State the blood parasite species.
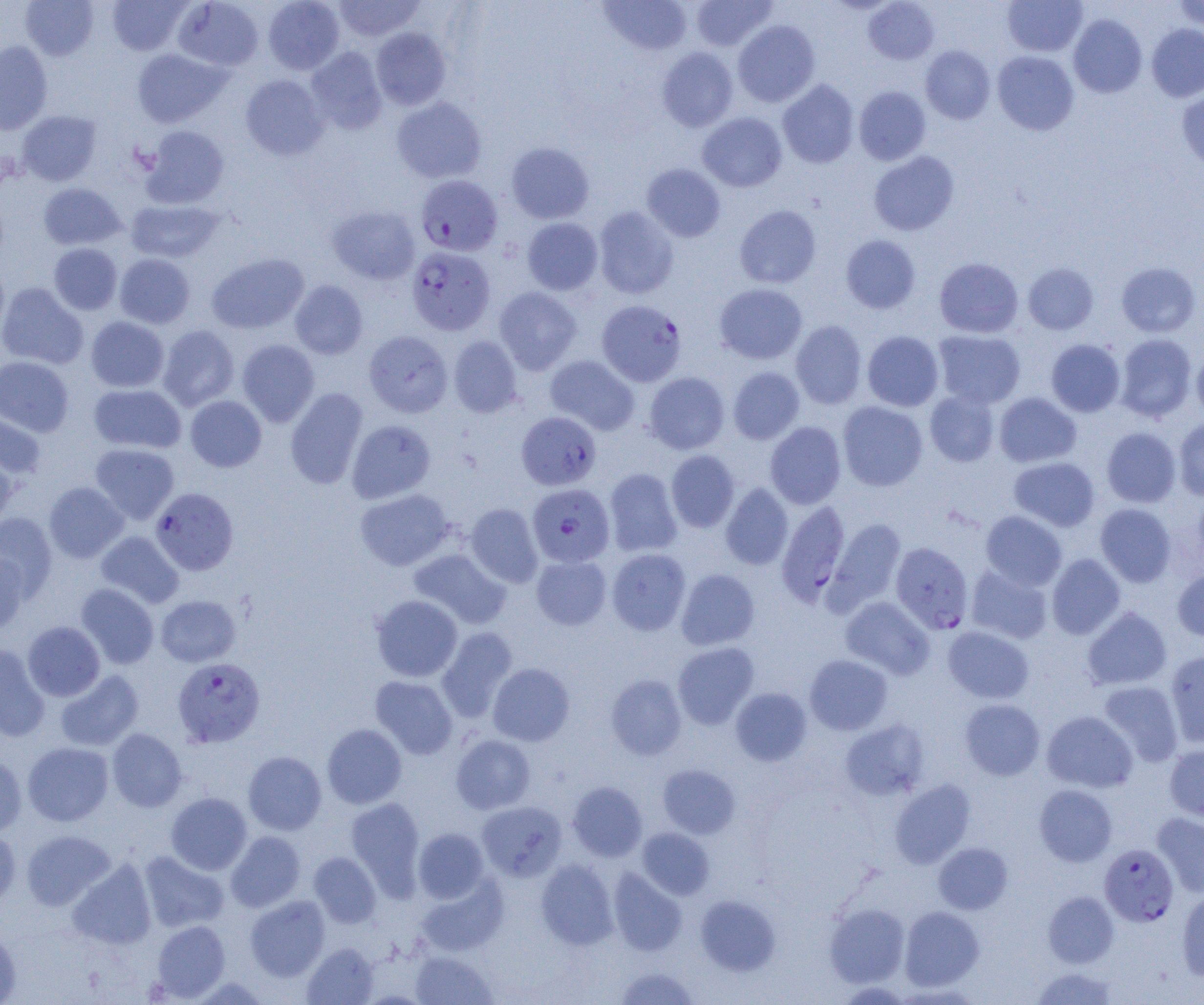

Plasmodium falciparum.

Summary:
  - Coordinate format: approximate bounding boxes as (x1,y1)-(x2,y2) corner pairs in pixels
  - Uninfected red blood cell locations: (20,0)-(99,60), (107,0)-(192,56), (263,0)-(344,74), (333,0)-(425,42), (689,0)-(777,51), (863,0)-(939,65), (1003,0)-(1088,57), (173,1)-(264,71), (599,1)-(693,56), (1173,1)-(1204,30), (1068,14)-(1147,98), (733,20)-(820,107), (1146,24)-(1204,103), (371,27)-(451,110), (0,41)-(53,135), (920,45)-(996,124), (306,46)-(387,134), (656,47)-(738,132), (132,49)-(229,127), (992,51)-(1079,135), (240,74)-(328,160), (777,79)-(859,168), (854,86)-(931,165), (1176,87)-(1204,170), (391,97)-(487,183), (17,111)-(101,186), (697,112)-(787,192), (141,125)-(230,209), (506,142)-(594,223), (869,151)-(960,236), (641,163)-(726,242), (38,183)-(127,250), (126,199)-(224,263), (593,205)-(679,299), (734,205)-(821,289), (326,206)-(420,285), (522,217)-(603,295), (840,234)-(921,314), (49,243)-(122,315), (207,253)-(309,334), (114,254)-(195,328), (934,257)-(1023,338), (1116,262)-(1201,337), (0,263)-(9,337), (1023,263)-(1098,335), (289,280)-(368,359), (0,283)-(88,370), (714,283)-(807,364), (494,286)-(582,375), (86,316)-(169,392), (791,320)-(867,409), (158,325)-(239,411), (363,330)-(453,418), (862,330)-(944,411), (933,330)-(1026,409), (1115,334)-(1197,422), (448,336)-(522,418), (237,339)-(320,426), (1045,339)-(1125,417), (1192,350)-(1204,421), (545,355)-(640,435), (0,356)-(74,437), (728,367)-(804,445), (644,372)-(730,454), (89,384)-(186,454), (285,387)-(368,490), (925,391)-(1000,467), (994,392)-(1081,468), (185,396)-(267,472), (838,401)-(928,491), (0,411)-(46,480), (1174,417)-(1204,500), (347,420)-(435,503), (765,421)-(846,509), (1101,427)-(1181,507), (90,443)-(179,524), (666,450)-(740,532), (0,455)-(16,533), (1009,457)-(1100,532), (604,468)-(682,557), (44,482)-(128,563), (720,483)-(793,570), (354,488)-(455,571), (1192,489)-(1204,568), (465,503)-(543,588), (1095,503)-(1176,587), (981,510)-(1067,590), (0,512)-(58,598), (825,518)-(907,614), (96,531)-(184,608), (606,548)-(691,636), (409,549)-(511,629), (0,551)-(30,635), (531,554)-(611,629), (1046,554)-(1125,639), (966,565)-(1053,644), (1172,568)-(1204,641), (676,569)-(759,650), (76,583)-(159,669), (156,595)-(241,667), (371,595)-(462,681), (840,597)-(934,679), (1082,606)-(1172,690), (22,621)-(105,701), (943,626)-(1034,703), (438,627)-(518,722), (672,642)-(759,729), (0,643)-(49,742), (1164,650)-(1204,747), (804,654)-(892,735), (487,663)-(575,746), (55,669)-(143,751), (605,674)-(687,760), (370,675)-(458,759), (1098,680)-(1184,767), (730,687)-(812,766), (960,698)-(1045,780), (1041,710)-(1138,793), (839,719)-(930,800), (322,724)-(407,809), (107,728)-(187,812), (451,734)-(536,814), (23,742)-(114,826), (1164,744)-(1204,822), (243,751)-(326,835), (0,755)-(27,838), (658,764)-(740,839), (888,779)-(975,868), (567,781)-(647,862), (1034,784)-(1117,867), (166,792)-(252,875), (346,797)-(425,894), (477,801)-(567,881), (1152,812)-(1204,897), (637,827)-(715,900), (413,828)-(489,903), (0,830)-(21,915), (21,830)-(116,910), (226,831)-(306,912), (933,842)-(1013,914), (138,851)-(229,932), (309,852)-(381,928), (67,859)-(157,950), (536,859)-(618,949), (608,867)-(687,956), (416,874)-(508,956), (1177,890)-(1204,981), (1043,891)-(1118,968), (695,894)-(781,975), (245,896)-(330,981), (824,903)-(910,987), (900,906)-(984,990), (151,920)-(230,1001), (0,929)-(21,1004), (302,942)-(378,1004), (410,951)-(498,1004), (614,966)-(700,1004), (1030,967)-(1119,1004)
  - Plasmodium falciparum-infected red blood cell locations: (416,175)-(502,256), (407,246)-(495,335), (596,300)-(687,387), (516,411)-(601,490), (527,483)-(615,567), (150,487)-(239,576), (776,500)-(851,607), (890,542)-(973,634), (173,657)-(265,748), (1099,843)-(1179,927)
  - Preparation: thin blood film
  - Modality: light microscopy
  - Magnification: 1000x
  - Image size: 1204×1005 pixels
  - Field of view: single